Assess this cell for malaria.
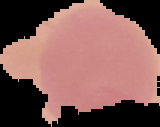

It is uninfected.

{
  "image_size": "160×127 pixels",
  "image_type": "segmented cell region on a black background",
  "preparation": "thin blood smear"
}